Classify this cell by malaria status.
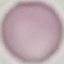

Uninfected.

Automatically extracted cell patch, resized to 64 × 64 pixels. Giemsa stain. Thin blood film. Photographed with a smartphone camera at the microscope eyepiece.